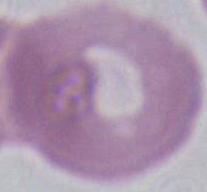

modality = micrograph
magnification = 1000x
identification = red blood cell